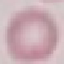

result = no malaria parasites detected
image type = automatically extracted cell patch, resized to 64 × 64 pixels
preparation = thin smear
stain = Giemsa
capture = smartphone through the microscope eyepiece